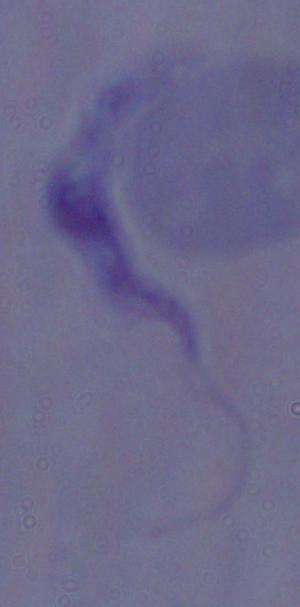 A trypanosome is seen. Micrograph. Captured at 1000x magnification.